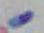
modality: micrograph
identification: Toxoplasma gondii
magnification: 1000x